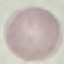
Malaria status: uninfected. Giemsa stain. Thin blood film. Automatically extracted cell patch, resized to 64 × 64 pixels. Acquired by smartphone through the microscope eyepiece.